Report the malaria status of this cell.
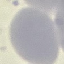

Uninfected.

Summary:
  - Stain: Giemsa
  - Preparation: thin blood smear
  - Image type: automatically extracted cell patch, resized to 64 × 64 pixels
  - Capture: smartphone camera at the microscope eyepiece